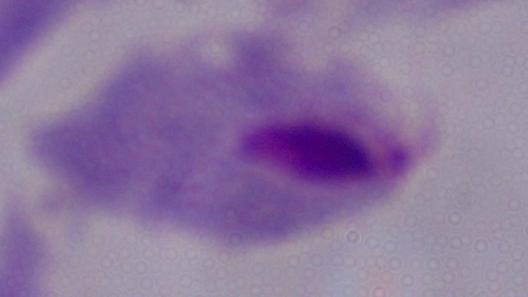 Micrograph. Captured at 1000x magnification. A trichomonad is seen.